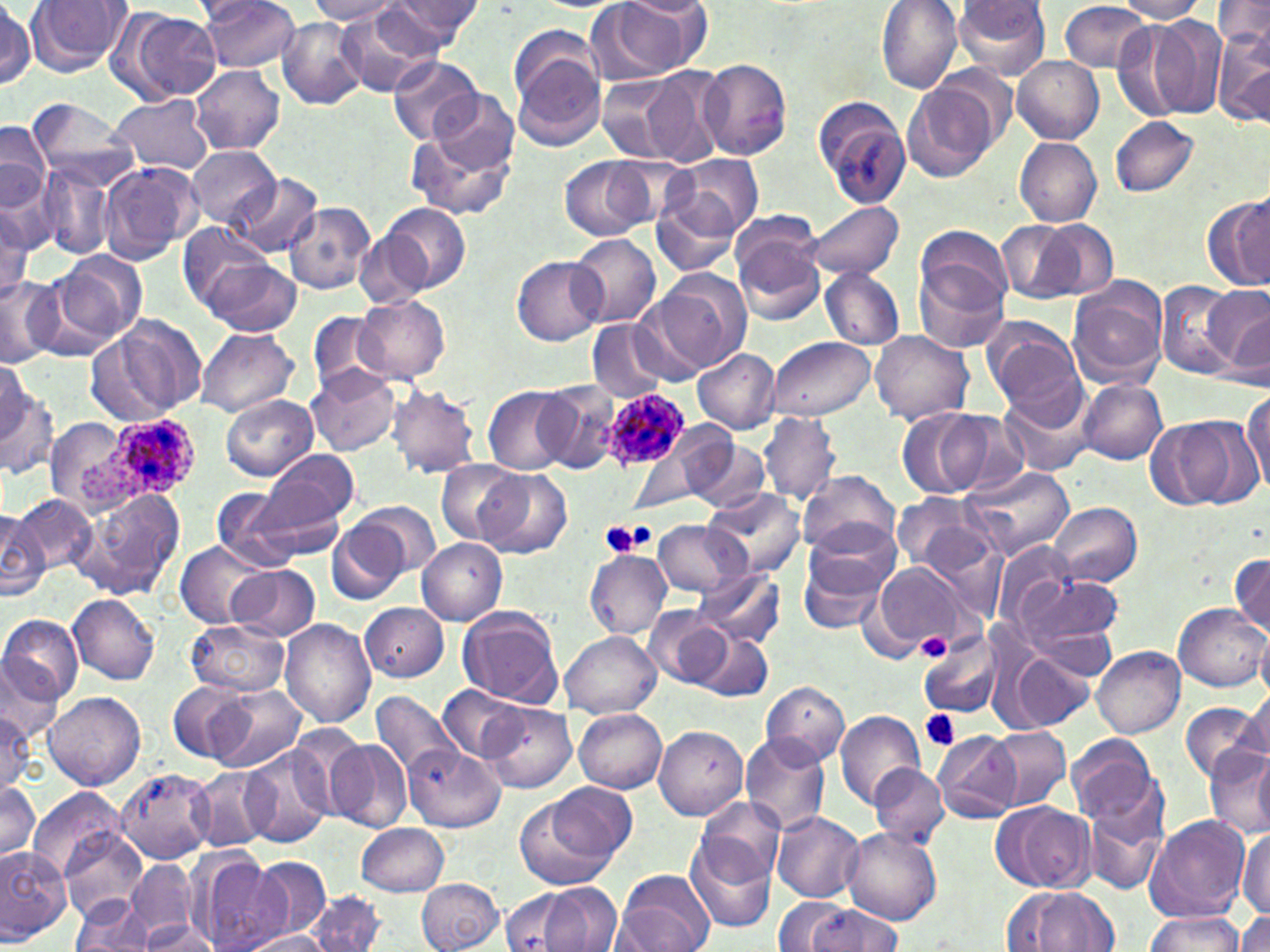

Summary:
  - Coordinate format: approximate bounding boxes as (x1,y1)-(x2,y2) corner pairs in pixels
  - Plasmodium ovale-infected red blood cell locations: (606,389)-(692,471), (78,419)-(198,503)
  - Uninfected red blood cell locations: (199,0)-(302,72), (380,0)-(481,52), (876,0)-(963,93), (1115,0)-(1208,22), (1214,0)-(1270,48), (26,1)-(132,75), (308,1)-(401,24), (588,1)-(705,82), (619,1)-(712,19), (953,1)-(1051,79), (1059,2)-(1152,72), (1,3)-(36,90), (335,6)-(446,98), (116,10)-(221,103), (1145,15)-(1227,119), (276,18)-(369,111), (1111,23)-(1192,121), (1212,29)-(1270,129), (509,42)-(609,153), (387,54)-(483,145), (1011,56)-(1103,143), (698,58)-(792,160), (640,65)-(727,165), (191,66)-(285,154), (599,73)-(690,162), (903,83)-(994,183), (421,89)-(520,183), (108,93)-(214,175), (813,95)-(914,209), (26,97)-(139,192), (1109,116)-(1200,198), (1,119)-(50,218), (406,119)-(517,222), (1015,138)-(1102,226), (186,147)-(282,229), (665,155)-(762,240), (559,157)-(655,242), (97,161)-(201,263), (35,164)-(114,260), (234,174)-(323,257), (651,191)-(742,277), (1206,195)-(1270,293), (1234,198)-(1267,286), (803,200)-(903,281), (282,202)-(375,294), (382,202)-(470,293), (0,209)-(32,299), (996,219)-(1092,304), (178,221)-(276,305), (731,221)-(825,325), (915,224)-(1013,312), (354,230)-(431,307), (569,234)-(661,328), (50,250)-(148,347), (202,257)-(302,337), (512,257)-(606,345), (915,260)-(1009,354), (820,268)-(906,351), (655,271)-(750,371), (0,273)-(64,368), (1068,277)-(1169,387), (1155,280)-(1240,376), (1199,283)-(1270,370), (629,293)-(724,385), (353,295)-(449,383), (1224,306)-(1269,390), (308,312)-(390,394), (93,316)-(205,422), (981,316)-(1084,419), (587,321)-(667,401), (195,329)-(299,417), (870,331)-(974,425), (765,335)-(875,420), (694,347)-(782,433), (0,364)-(43,444), (308,365)-(401,456), (0,376)-(58,480), (1079,378)-(1167,465), (535,380)-(628,476), (999,382)-(1098,477), (387,384)-(481,478), (484,386)-(572,474), (1243,390)-(1270,496), (220,394)-(317,482), (895,407)-(997,499), (759,411)-(840,505), (936,411)-(1033,499), (42,416)-(134,512), (1145,417)-(1237,509), (676,428)-(771,510), (261,448)-(359,529), (627,448)-(702,513), (436,459)-(523,546), (239,465)-(354,563), (960,465)-(1077,560), (475,468)-(570,558), (799,471)-(900,559), (212,487)-(294,567), (706,487)-(803,576), (66,488)-(187,601), (890,493)-(995,579), (14,495)-(95,574), (1046,501)-(1140,588), (356,502)-(441,577), (0,507)-(50,600), (326,519)-(408,604), (652,519)-(749,598), (798,529)-(897,631), (416,538)-(507,625), (176,540)-(271,628), (991,542)-(1076,625), (584,549)-(672,638), (1230,552)-(1270,638), (869,561)-(973,654), (230,565)-(320,641), (692,567)-(786,648), (1007,570)-(1126,666), (68,593)-(160,685), (360,602)-(449,682), (1173,602)-(1270,691), (456,605)-(563,708), (644,606)-(729,688), (0,614)-(84,705), (187,619)-(289,696), (280,619)-(375,727), (1254,625)-(1270,702), (918,628)-(1006,719), (693,631)-(775,702), (561,632)-(661,718), (1091,646)-(1185,737), (0,649)-(69,739), (1008,650)-(1094,732), (759,680)-(850,768), (168,681)-(254,763), (207,685)-(308,772), (441,686)-(525,762), (1241,689)-(1270,765), (43,691)-(144,791), (368,691)-(466,784), (479,701)-(576,793), (1180,702)-(1266,783), (1,704)-(36,791), (574,708)-(667,793), (835,710)-(925,812), (654,724)-(748,820), (986,728)-(1069,808), (933,729)-(1021,823), (738,733)-(830,835), (1066,734)-(1163,831), (326,737)-(413,832), (401,743)-(505,831), (240,745)-(334,848), (1206,749)-(1270,840), (1253,750)-(1270,833), (870,764)-(949,847), (190,765)-(276,852), (116,767)-(217,864), (1,779)-(39,863), (547,780)-(636,866), (27,789)-(125,881), (514,796)-(622,891), (695,796)-(786,886), (1083,796)-(1166,897), (992,801)-(1095,894), (772,810)-(865,903), (1144,815)-(1250,922), (357,823)-(450,896), (57,826)-(150,920), (1237,826)-(1269,919), (842,828)-(941,926), (684,834)-(777,933), (0,847)-(71,943), (190,852)-(290,952), (250,856)-(333,939), (126,859)-(197,944), (614,869)-(714,952), (416,878)-(504,952), (536,884)-(623,951), (1002,886)-(1121,951), (500,887)-(589,952), (307,890)-(386,952), (70,897)-(155,951), (773,897)-(854,948), (806,903)-(904,952), (1233,909)-(1270,952), (1144,911)-(1245,951), (139,923)-(222,951), (241,931)-(334,951)
  - Platelet locations: (598,519)-(656,559), (916,632)-(951,660), (921,709)-(962,753)
  - Slide-level diagnosis: Plasmodium ovale
  - Image size: 1270×952 pixels
  - Field of view: one of a larger specimen
  - Stain: May-Grünwald-Giemsa
  - Preparation: thin blood smear
  - Modality: light microscopy
  - Magnification: 1000x